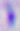 Captured at 400x magnification. Toxoplasma gondii is shown. Photomicrograph.